Name the parasite shown.
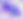
This is Toxoplasma gondii.

magnification = 400x
modality = photomicrograph